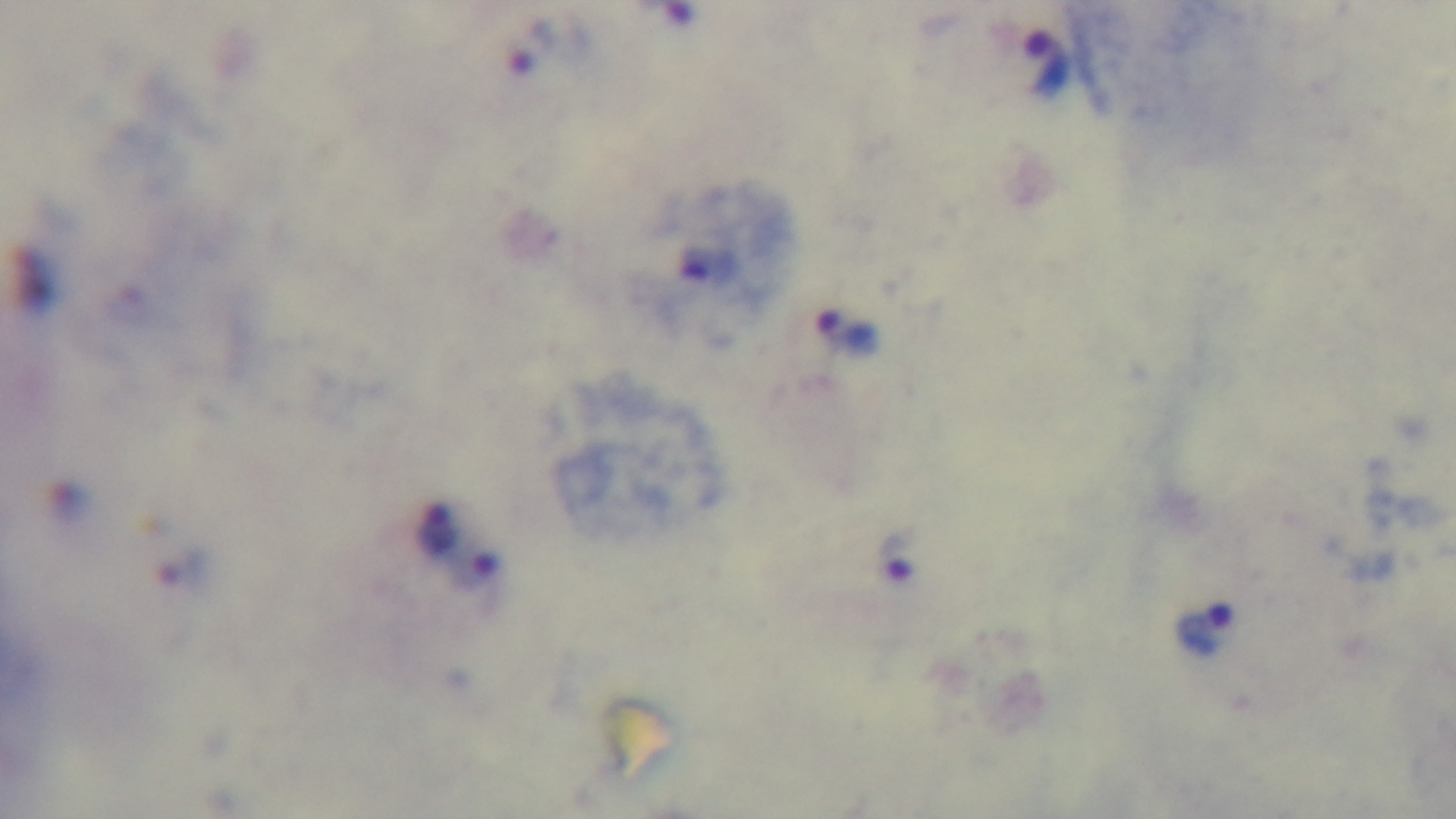
Summary:
  - Objective: 100x oil immersion
  - Stain: Giemsa
  - Preparation: thick smear
  - Modality: light microscopy
  - Capture: mounted 4K digital camera
  - Field of view: one from the slide
  - Malaria status: positive